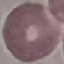

{
  "result": "negative for malaria parasites",
  "image_type": "cell patch, automatically extracted from a larger field of view and resized to 64 × 64 pixels",
  "capture": "smartphone through the microscope eyepiece",
  "preparation": "thin smear",
  "stain": "Giemsa"
}